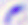 Toxoplasma gondii is shown. Photomicrograph. 400x magnification.